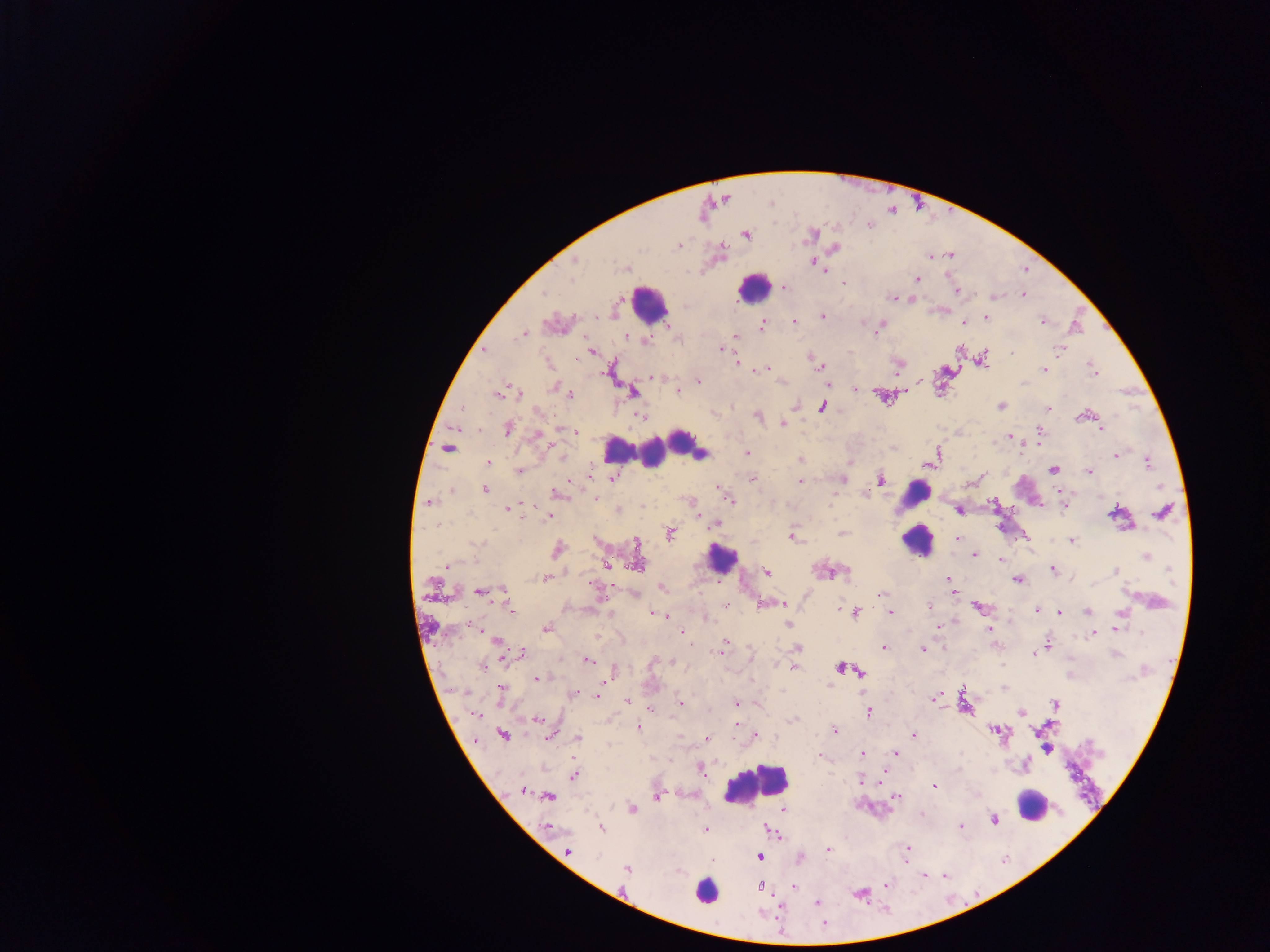
capture = mobile-phone photograph through a microscope
image size = 1270×952 pixels
leukocyte locations = approximate centers as (x, y) in pixels: (757, 288), (656, 301), (680, 439), (665, 446), (616, 448), (651, 454), (1029, 491), (916, 493), (917, 541), (722, 559), (756, 772), (1041, 805), (708, 884)
object labeled both malaria parasite and leukocyte by the source = approximate centers as (x, y) in pixels: (699, 452)
preparation = thick blood smear
country = Ghana
field of view = single
malaria parasite locations = approximate centers as (x, y) in pixels: (813, 234), (746, 235), (678, 245), (835, 248), (930, 256), (949, 256), (575, 261), (813, 261), (821, 267), (625, 269), (571, 278), (917, 279), (844, 283), (784, 288), (957, 291), (542, 294), (1023, 295), (994, 297), (892, 298), (822, 316), (987, 318), (1042, 320), (794, 322), (964, 323), (762, 325), (878, 331), (524, 334), (735, 335), (626, 336), (647, 341), (721, 349), (1060, 349), (484, 351), (591, 351), (1012, 354), (983, 359), (737, 363), (818, 366), (762, 369), (1044, 370), (1094, 371), (651, 378), (699, 382), (781, 382), (552, 386), (855, 388), (678, 391), (633, 393), (499, 394), (520, 395), (570, 395), (795, 406), (823, 406), (1001, 406), (1048, 409), (642, 416), (758, 416), (1079, 417), (782, 424), (1101, 428), (508, 429), (1040, 430), (575, 432), (1010, 436), (538, 437), (1036, 442), (448, 449), (747, 452), (1115, 456), (800, 459), (488, 462), (1148, 463), (930, 464), (1053, 469), (519, 470), (1088, 472), (981, 476), (613, 478), (753, 478), (843, 480), (881, 480), (800, 481), (718, 488), (485, 489), (451, 492), (721, 492), (558, 493), (863, 494), (595, 498), (730, 501), (428, 502), (994, 504), (529, 506), (1064, 506), (507, 508), (618, 510), (959, 511), (1113, 512), (1161, 512), (548, 518), (437, 525), (716, 525), (670, 533), (842, 533), (792, 537), (957, 539), (1071, 541), (557, 549), (974, 555), (1147, 556), (1000, 560), (446, 565), (606, 565), (637, 565), (1053, 570), (1170, 570), (1116, 571), (767, 572), (827, 572), (545, 578), (949, 579), (1017, 580), (594, 586), (663, 587), (953, 590), (504, 591), (479, 592), (883, 594), (782, 602), (727, 604), (929, 605), (978, 607), (511, 609), (838, 609), (1036, 610), (891, 612), (1059, 612), (1087, 612), (653, 613), (855, 613), (665, 615), (707, 619), (788, 624), (938, 626), (546, 628), (990, 628), (1115, 629), (682, 632), (1140, 633), (1093, 634), (801, 635), (495, 640), (724, 642), (1048, 645), (883, 649), (923, 649), (719, 652), (522, 653), (1033, 654), (588, 660), (673, 662), (1002, 665), (482, 666), (794, 668), (841, 668), (615, 670), (859, 671), (537, 678), (501, 689), (600, 690), (575, 693), (598, 695), (932, 699), (627, 700), (681, 703), (736, 703), (1054, 704), (651, 709), (1019, 712), (869, 713), (476, 715), (538, 720), (792, 720), (736, 724), (638, 728), (834, 730), (996, 730), (503, 735), (756, 735), (913, 736), (549, 737), (578, 738), (707, 739), (1047, 749), (895, 753), (862, 754), (819, 757), (702, 773), (574, 776), (860, 780), (935, 785), (522, 790), (548, 796), (897, 796), (656, 797), (632, 808), (784, 810), (993, 819), (960, 826), (547, 827), (601, 828), (705, 829), (775, 834), (827, 849), (568, 850), (907, 850), (598, 856), (760, 858), (712, 861), (627, 868), (924, 876), (887, 883), (760, 887), (793, 887), (817, 903)